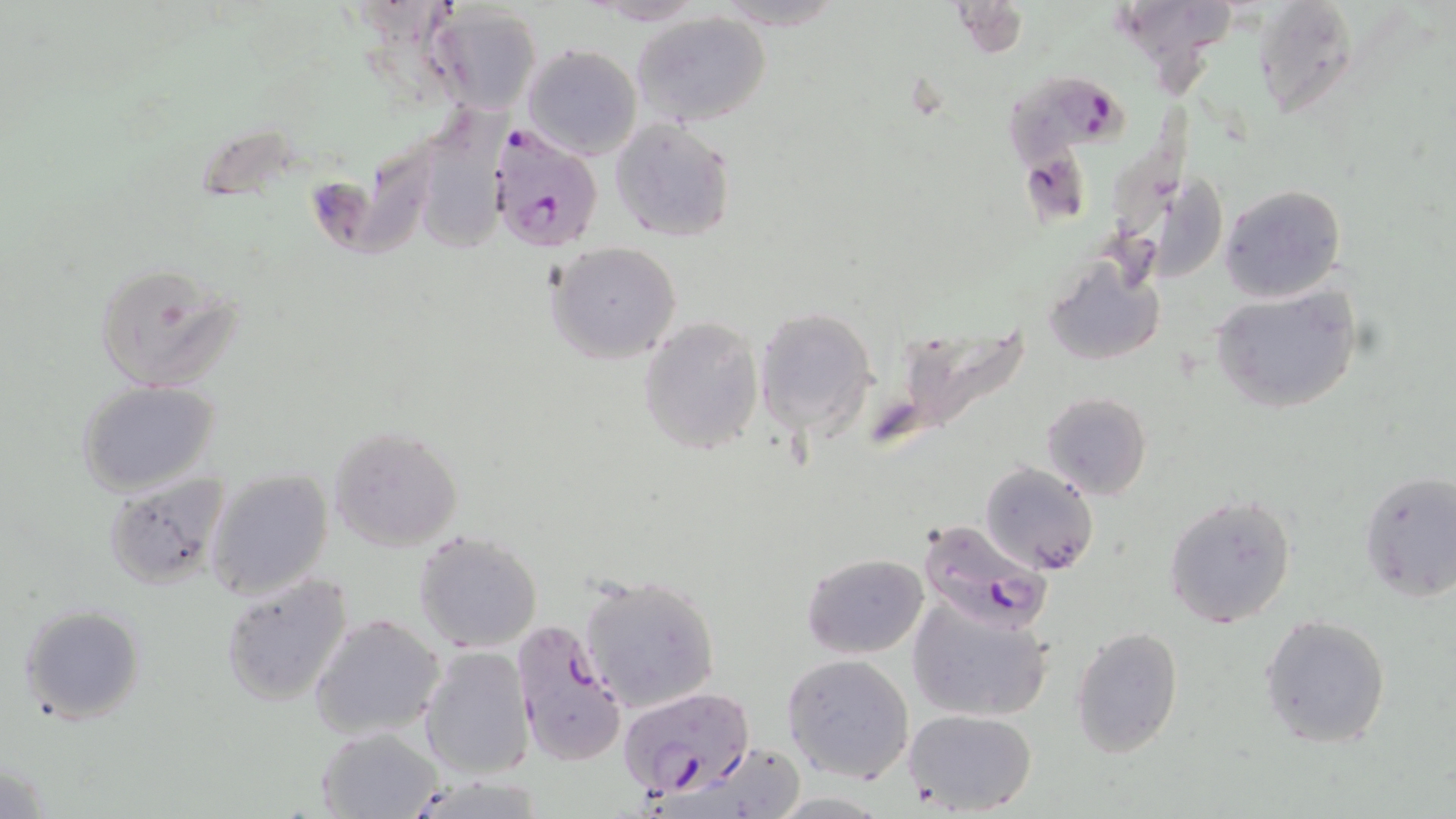
{
  "plasmodium_falciparum_infected_red_blood_cell_locations": "approximate bounding boxes as [x1, y1, x2, y2] in pixels: [1005, 71, 1142, 221], [485, 124, 606, 253], [916, 516, 1053, 634], [508, 617, 628, 770], [619, 687, 753, 802]",
  "slide_level_diagnosis": "Plasmodium falciparum",
  "uninfected_red_blood_cell_locations": "approximate bounding boxes as [x1, y1, x2, y2] in pixels: [582, 0, 709, 24], [1108, 0, 1237, 91], [1252, 1, 1360, 118], [430, 3, 542, 112], [632, 12, 772, 127], [520, 43, 643, 160], [426, 100, 521, 261], [611, 118, 736, 242], [311, 139, 444, 261], [1116, 152, 1229, 284], [1218, 182, 1348, 304], [547, 242, 682, 362], [1044, 252, 1166, 370], [91, 261, 246, 393], [1209, 285, 1363, 415], [755, 308, 876, 433], [638, 316, 765, 456], [872, 322, 1034, 455], [77, 380, 221, 496], [1041, 391, 1153, 500], [327, 426, 463, 552], [979, 461, 1100, 574], [206, 467, 334, 599], [1357, 468, 1456, 602], [104, 473, 235, 591], [1163, 493, 1298, 629], [413, 529, 544, 653], [801, 552, 928, 658], [576, 571, 721, 715], [219, 573, 354, 708], [906, 593, 1053, 722], [18, 604, 147, 724], [308, 612, 444, 741], [1259, 613, 1392, 749], [1069, 624, 1183, 759], [420, 646, 534, 780], [782, 653, 914, 784], [902, 707, 1037, 815], [316, 727, 442, 818]",
  "preparation": "thin blood smear",
  "stain": "May-Grünwald-Giemsa",
  "modality": "optical microscopy",
  "image_size": "1456×819 pixels",
  "field_of_view": "single",
  "magnification": "1000x"
}